Point out each Plasmodium parasite.
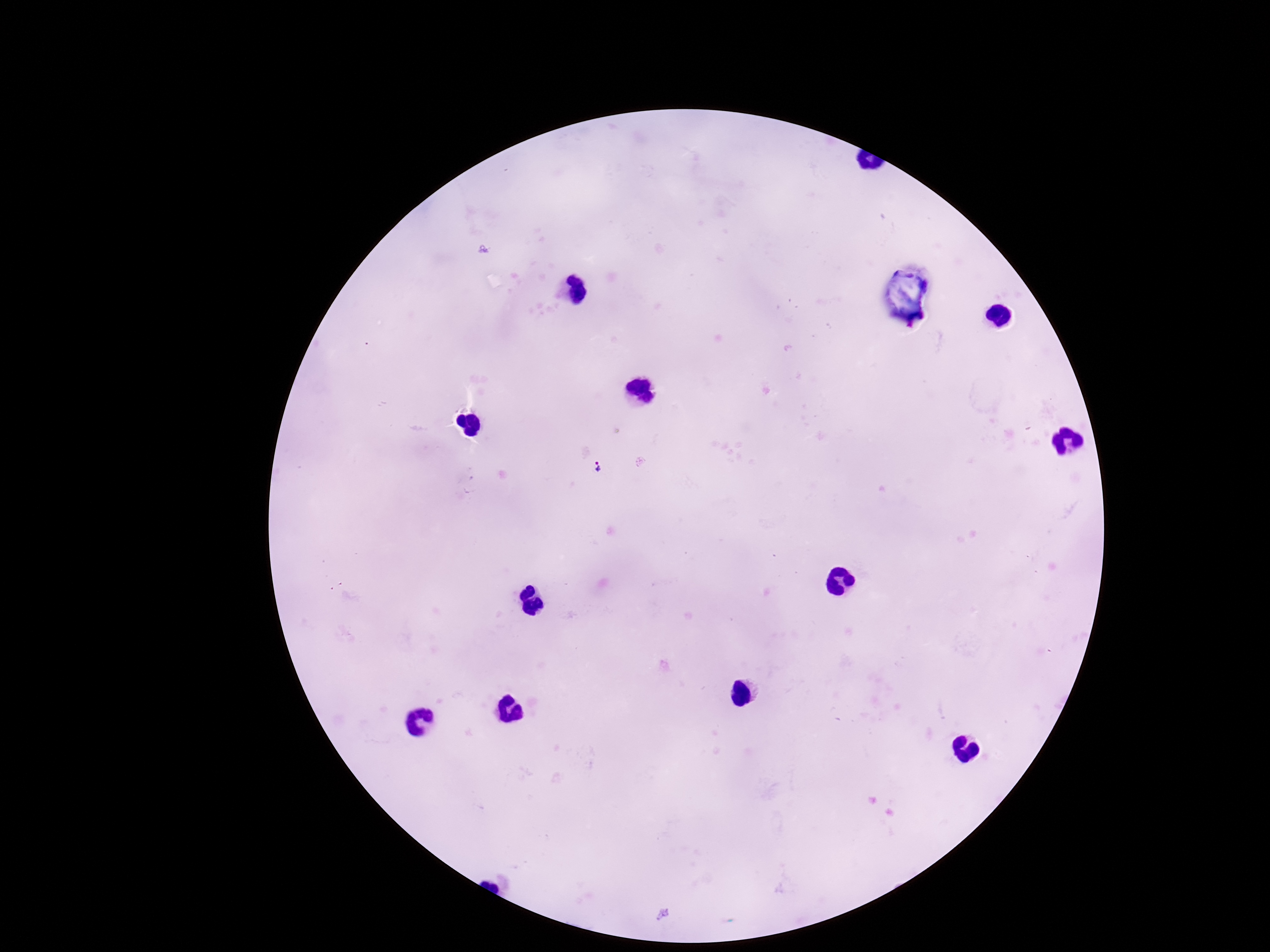
Approximate object centers, in pixels from the top-left corner.
Plasmodium parasites: (x=597, y=468).

Photographed through the microscope eyepiece with a smartphone camera. Giemsa stain. Thick blood film. One field from this slide. Patient malaria status: infected. 100x magnification. Image is 1270×952 pixels.